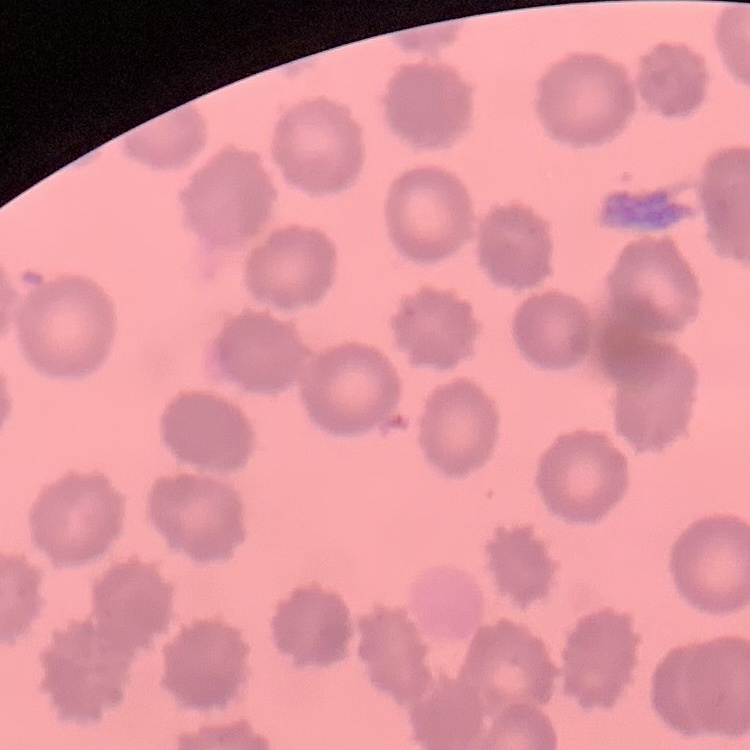
red blood cell morphology = no rouleaux formation
stain = Field's or Giemsa
image type = one tile cut from a larger photomicrograph
preparation = thin blood film